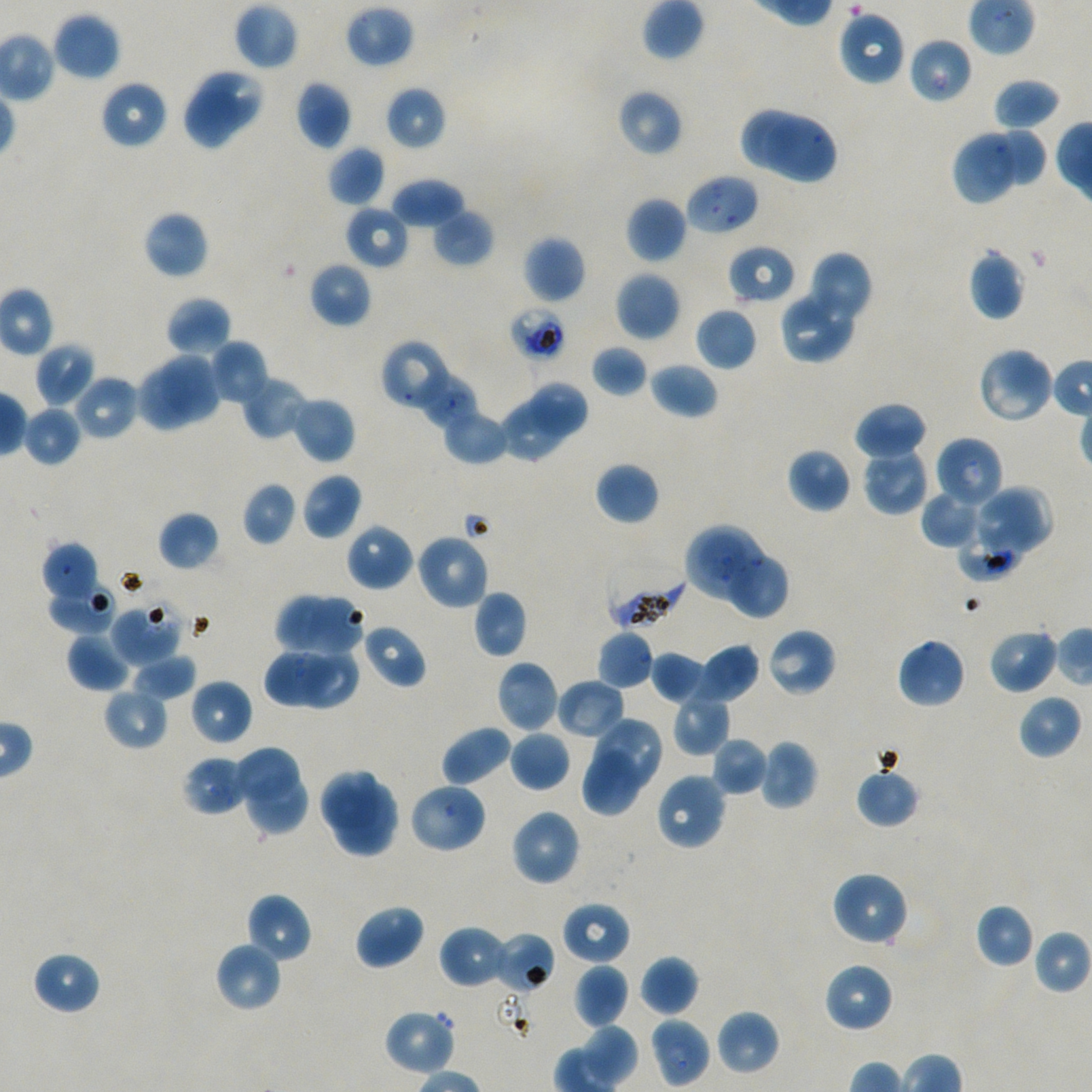
Approximate bounding boxes as (x1, y1, x2, y2) in pixels. Not every red blood cell is marked. Locations of uninfected red blood cells: (233, 2, 299, 71), (344, 5, 414, 68), (837, 10, 907, 87), (52, 12, 121, 81), (198, 71, 261, 132), (992, 77, 1061, 131), (100, 79, 168, 149), (295, 80, 352, 150), (385, 86, 446, 150), (616, 89, 683, 157), (185, 90, 242, 149), (743, 110, 799, 168), (766, 117, 835, 184), (995, 129, 1046, 185), (956, 133, 1018, 202), (327, 145, 385, 208), (390, 178, 466, 228), (625, 196, 687, 264), (346, 204, 410, 270), (431, 208, 494, 267), (142, 210, 209, 280), (522, 234, 586, 304), (967, 249, 1025, 321), (807, 251, 873, 325), (308, 261, 372, 328), (615, 270, 681, 342), (778, 290, 857, 364), (165, 295, 232, 357), (695, 307, 757, 371), (380, 338, 454, 412), (209, 340, 269, 405), (35, 342, 95, 408), (590, 345, 649, 397), (977, 346, 1055, 425), (160, 352, 219, 421), (649, 361, 718, 420), (135, 370, 194, 431), (72, 374, 139, 441), (240, 375, 310, 441), (530, 381, 587, 436), (291, 396, 355, 464), (498, 400, 566, 463), (854, 401, 927, 461), (22, 405, 82, 466), (442, 408, 511, 465), (936, 436, 1004, 509), (786, 447, 852, 513), (861, 447, 930, 516), (595, 462, 659, 526), (301, 472, 363, 541), (242, 481, 296, 545), (972, 486, 1053, 557), (920, 490, 985, 549), (158, 511, 220, 571), (346, 523, 414, 592), (415, 532, 490, 610), (41, 542, 99, 604), (729, 555, 790, 619), (50, 584, 115, 632), (473, 590, 528, 658), (274, 592, 329, 651), (308, 598, 363, 654), (110, 603, 183, 665), (363, 624, 426, 688), (765, 627, 837, 697), (988, 627, 1059, 694), (596, 630, 655, 690), (66, 632, 132, 692), (897, 637, 966, 709), (695, 643, 760, 704), (302, 648, 359, 708), (651, 650, 708, 704), (263, 651, 321, 706), (130, 653, 196, 702), (495, 661, 560, 733), (189, 678, 253, 746), (556, 678, 626, 740), (103, 687, 168, 750), (672, 693, 730, 755), (1017, 694, 1082, 760), (594, 718, 662, 792), (441, 725, 513, 786), (509, 729, 570, 792), (710, 736, 769, 796), (759, 739, 817, 809), (234, 748, 299, 802), (582, 749, 638, 816), (181, 754, 249, 816), (855, 766, 920, 828), (321, 771, 378, 829), (655, 772, 728, 852), (247, 773, 310, 833), (408, 782, 488, 854), (344, 783, 397, 835), (335, 801, 392, 856), (509, 807, 581, 886), (830, 871, 909, 947), (245, 893, 312, 965), (561, 900, 631, 965), (975, 903, 1036, 968), (354, 904, 426, 970), (439, 925, 510, 989), (215, 941, 283, 1013), (31, 950, 101, 1015), (639, 954, 699, 1017), (823, 962, 894, 1034), (573, 964, 630, 1029), (382, 1008, 456, 1076), (715, 1008, 780, 1076), (582, 1023, 638, 1087). Locations of infected red blood cells: (685, 174, 761, 236), (604, 564, 685, 630). Locations of red blood cells of indeterminate infection status: (909, 37, 972, 105), (727, 244, 797, 305), (509, 306, 566, 362), (416, 372, 477, 429), (685, 525, 770, 607), (956, 532, 1022, 582), (494, 931, 555, 995), (649, 1016, 711, 1088). Blood group of the donor: A+/O+. Image is 1092×1092 pixels. 100x objective under oil immersion, numerical aperture 1.45. Thin blood film. Giemsa stain. Single field of view. P. falciparum strain NF54 in static in-vitro culture.